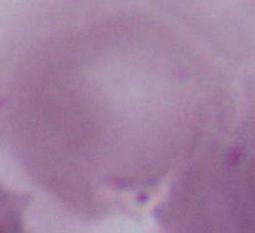

Summary:
  - Modality: photomicrograph
  - Identification: erythrocyte
  - Magnification: 1000x